Give the extent of all Babesia divergens-infected red blood cells.
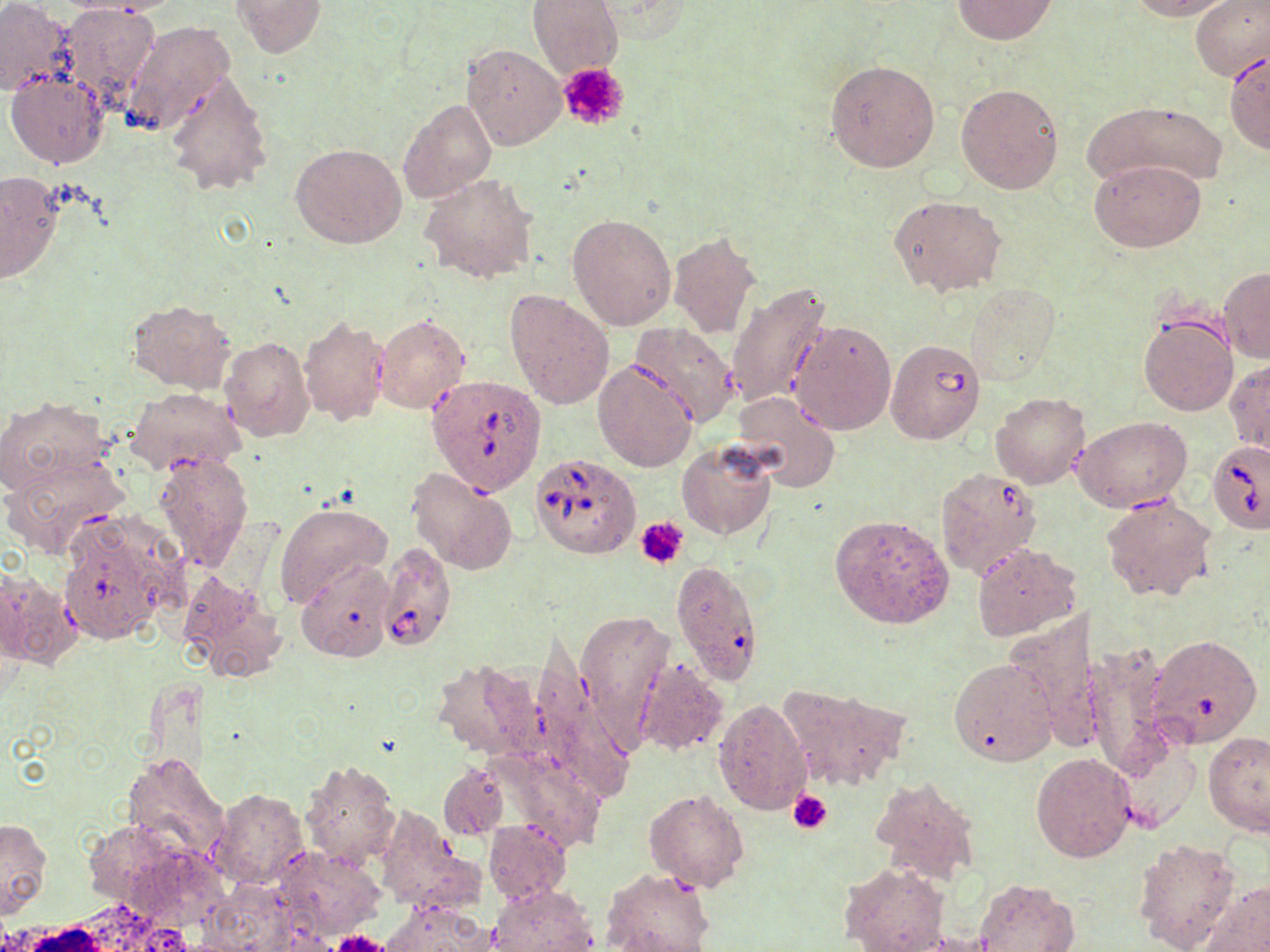
Approximate bounding boxes as named x1/y1/x2/y2 corners in pixels.
Babesia divergens-infected red blood cells: (x1=885, y1=337, x2=987, y2=445), (x1=428, y1=375, x2=546, y2=494), (x1=1207, y1=439, x2=1270, y2=535), (x1=531, y1=451, x2=640, y2=559), (x1=379, y1=542, x2=456, y2=653).

slide_level_diagnosis: Babesia divergens
magnification: 1000x
modality: optical microscopy
field_of_view: one of a larger specimen
preparation: thin blood film
stain: May-Grünwald-Giemsa
image_size: 1270×952 pixels
platelet_locations: 'approximate bounding boxes as named x1/y1/x2/y2 corners in pixels: (x1=559, y1=61, x2=630, y2=131), (x1=638, y1=518, x2=688, y2=568), (x1=788, y1=790, x2=833, y2=835), (x1=331, y1=930, x2=390, y2=952)'
uninfected_red_blood_cell_locations: 'approximate bounding boxes as named x1/y1/x2/y2 corners in pixels: (x1=0, y1=0, x2=78, y2=95), (x1=60, y1=0, x2=178, y2=17), (x1=232, y1=0, x2=326, y2=57), (x1=527, y1=0, x2=623, y2=80), (x1=950, y1=0, x2=1058, y2=43), (x1=1128, y1=0, x2=1234, y2=20), (x1=1189, y1=0, x2=1270, y2=81), (x1=60, y1=3, x2=158, y2=104), (x1=122, y1=21, x2=235, y2=135), (x1=462, y1=42, x2=566, y2=150), (x1=1224, y1=52, x2=1270, y2=153), (x1=824, y1=59, x2=940, y2=172), (x1=164, y1=70, x2=273, y2=198), (x1=6, y1=71, x2=109, y2=168), (x1=956, y1=83, x2=1064, y2=193), (x1=399, y1=99, x2=496, y2=204), (x1=1087, y1=99, x2=1227, y2=189), (x1=290, y1=142, x2=408, y2=250), (x1=1090, y1=159, x2=1206, y2=251), (x1=1, y1=172, x2=66, y2=285), (x1=420, y1=173, x2=539, y2=285), (x1=887, y1=194, x2=1006, y2=297), (x1=567, y1=213, x2=677, y2=330), (x1=667, y1=232, x2=762, y2=339), (x1=1219, y1=269, x2=1270, y2=362), (x1=727, y1=284, x2=834, y2=409), (x1=963, y1=284, x2=1058, y2=384), (x1=505, y1=288, x2=616, y2=410), (x1=126, y1=300, x2=236, y2=393), (x1=1138, y1=311, x2=1238, y2=416), (x1=374, y1=314, x2=469, y2=414), (x1=298, y1=315, x2=390, y2=426), (x1=789, y1=320, x2=897, y2=436), (x1=631, y1=322, x2=739, y2=427), (x1=218, y1=336, x2=314, y2=442), (x1=1226, y1=358, x2=1269, y2=454), (x1=593, y1=359, x2=697, y2=473), (x1=125, y1=386, x2=247, y2=475), (x1=991, y1=391, x2=1090, y2=489), (x1=732, y1=392, x2=841, y2=491), (x1=1, y1=397, x2=113, y2=495), (x1=1075, y1=417, x2=1192, y2=511), (x1=677, y1=439, x2=777, y2=541), (x1=3, y1=450, x2=129, y2=556), (x1=152, y1=452, x2=254, y2=571), (x1=406, y1=468, x2=517, y2=575), (x1=936, y1=468, x2=1043, y2=578), (x1=1103, y1=492, x2=1217, y2=603), (x1=275, y1=502, x2=392, y2=607), (x1=57, y1=513, x2=182, y2=642), (x1=829, y1=514, x2=954, y2=630), (x1=972, y1=543, x2=1079, y2=640), (x1=295, y1=559, x2=396, y2=662), (x1=670, y1=559, x2=765, y2=684), (x1=1, y1=565, x2=77, y2=671), (x1=175, y1=570, x2=287, y2=680), (x1=577, y1=609, x2=673, y2=736), (x1=1144, y1=634, x2=1262, y2=748), (x1=1083, y1=640, x2=1175, y2=782), (x1=434, y1=657, x2=548, y2=762), (x1=635, y1=658, x2=727, y2=757), (x1=948, y1=658, x2=1057, y2=766), (x1=778, y1=682, x2=910, y2=790), (x1=713, y1=696, x2=813, y2=816), (x1=1202, y1=730, x2=1270, y2=837), (x1=1112, y1=732, x2=1201, y2=835), (x1=1031, y1=752, x2=1137, y2=862), (x1=121, y1=753, x2=228, y2=865), (x1=299, y1=759, x2=400, y2=868), (x1=439, y1=762, x2=509, y2=840), (x1=869, y1=775, x2=981, y2=887), (x1=210, y1=788, x2=309, y2=888), (x1=644, y1=790, x2=750, y2=892), (x1=373, y1=809, x2=481, y2=913), (x1=0, y1=818, x2=53, y2=915), (x1=484, y1=820, x2=572, y2=903), (x1=1133, y1=838, x2=1241, y2=952), (x1=841, y1=861, x2=950, y2=952), (x1=600, y1=867, x2=716, y2=952), (x1=972, y1=878, x2=1078, y2=951), (x1=1202, y1=882, x2=1270, y2=951), (x1=488, y1=884, x2=598, y2=952), (x1=381, y1=900, x2=496, y2=952)'